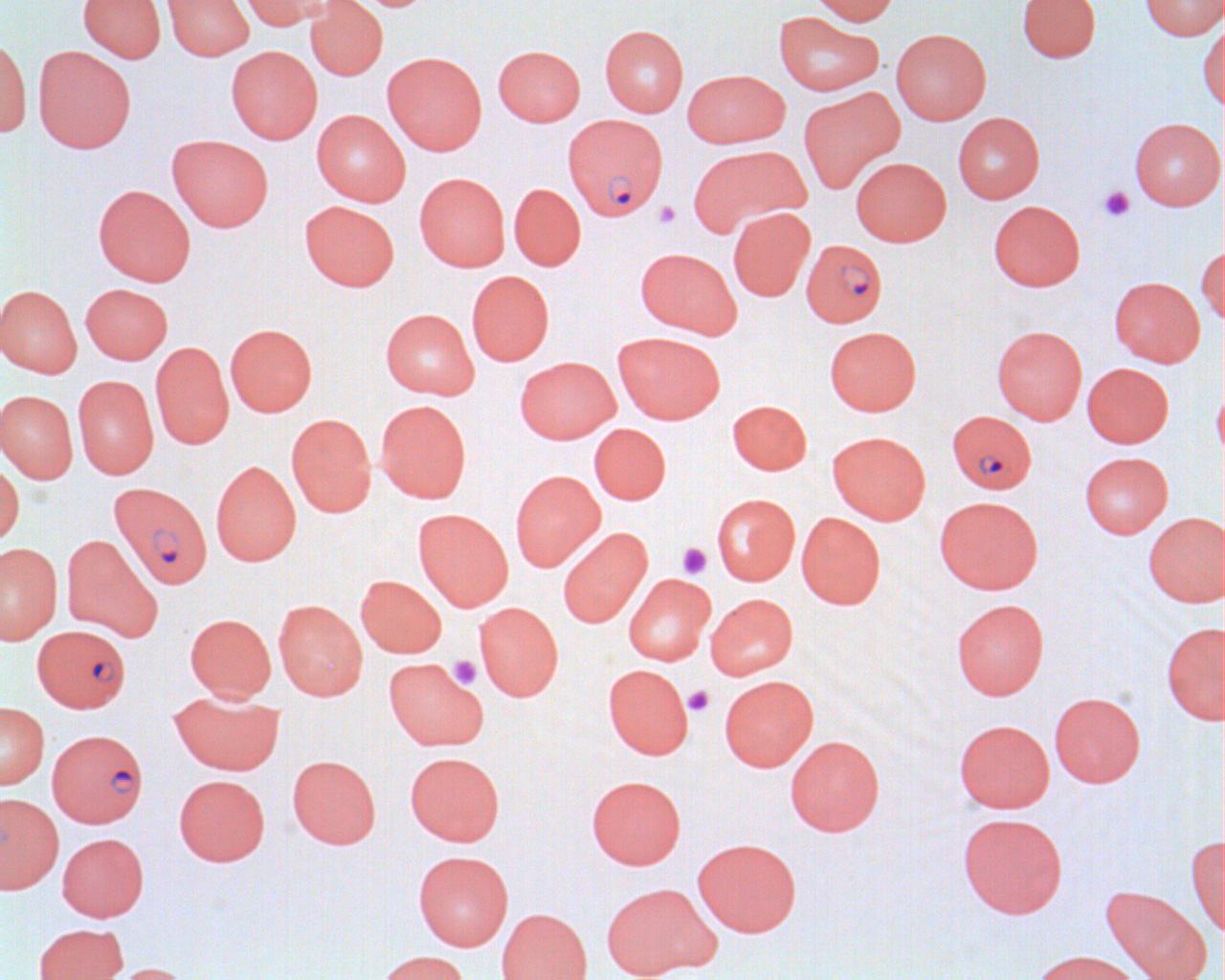
Summary:
  - Coordinate format: approximate bounding boxes as (x1,y1)-(x2,y2) corner pairs in pixels
  - Uninfected red blood cell locations: (78,0)-(166,63), (162,0)-(254,61), (237,0)-(331,30), (305,0)-(388,80), (808,0)-(900,25), (1017,0)-(1100,62), (1139,0)-(1225,40), (774,11)-(885,96), (1198,19)-(1225,112), (600,24)-(688,117), (891,29)-(991,124), (0,33)-(32,138), (493,44)-(585,126), (33,46)-(137,153), (226,46)-(323,144), (382,51)-(487,155), (682,69)-(789,148), (799,87)-(905,192), (311,110)-(410,206), (953,112)-(1044,203), (1129,117)-(1224,210), (167,134)-(274,231), (689,145)-(810,236), (851,157)-(951,246), (414,172)-(510,271), (509,183)-(586,271), (93,184)-(196,286), (300,200)-(400,291), (988,200)-(1085,291), (728,207)-(815,301), (1197,244)-(1224,327), (636,247)-(741,338), (466,270)-(554,366), (1109,277)-(1205,367), (81,283)-(173,364), (0,285)-(82,378), (380,309)-(479,399), (225,323)-(317,416), (825,326)-(921,415), (992,326)-(1087,424), (613,332)-(725,424), (151,342)-(234,449), (515,356)-(620,443), (1082,363)-(1174,448), (73,376)-(159,479), (1212,380)-(1225,465), (0,390)-(78,483), (375,399)-(472,503), (727,399)-(811,474), (286,413)-(376,517), (589,423)-(671,504), (827,431)-(930,524), (1079,451)-(1173,538), (211,460)-(301,566), (0,461)-(24,547), (509,470)-(605,571), (711,493)-(799,585), (934,496)-(1043,594), (413,508)-(513,610), (797,512)-(885,609), (1143,512)-(1225,607), (558,527)-(652,627), (61,534)-(163,642), (0,543)-(62,644), (624,573)-(715,665), (356,575)-(447,657), (705,593)-(798,680), (952,598)-(1049,699), (273,600)-(367,699), (474,602)-(563,701), (185,613)-(276,701), (1161,621)-(1225,724), (383,657)-(488,751), (603,664)-(693,759), (719,675)-(818,771), (169,690)-(283,774), (1049,692)-(1145,787), (0,702)-(49,789), (953,718)-(1054,813), (785,735)-(884,835), (405,752)-(505,846), (288,754)-(381,848), (174,774)-(269,866), (586,775)-(686,869), (0,793)-(63,893), (958,812)-(1067,918), (57,832)-(148,921), (1186,835)-(1225,938), (693,838)-(801,936), (413,850)-(513,950), (601,883)-(715,979), (1100,885)-(1211,980), (496,908)-(591,980), (34,923)-(128,980), (1029,949)-(1143,980), (374,950)-(470,980), (103,962)-(194,980)
  - Plasmodium falciparum-infected red blood cell locations: (566,115)-(671,221), (801,239)-(887,327), (947,410)-(1037,494), (110,482)-(215,589), (32,625)-(130,712), (47,729)-(148,827)
  - Platelet locations: (1098,186)-(1135,221), (654,200)-(680,228), (677,543)-(711,578), (448,655)-(481,688), (683,685)-(714,715)
  - Slide-level diagnosis: Plasmodium falciparum
  - Magnification: 1000x
  - Field of view: single
  - Modality: optical microscopy
  - Preparation: thin blood film
  - Image size: 1225×980 pixels